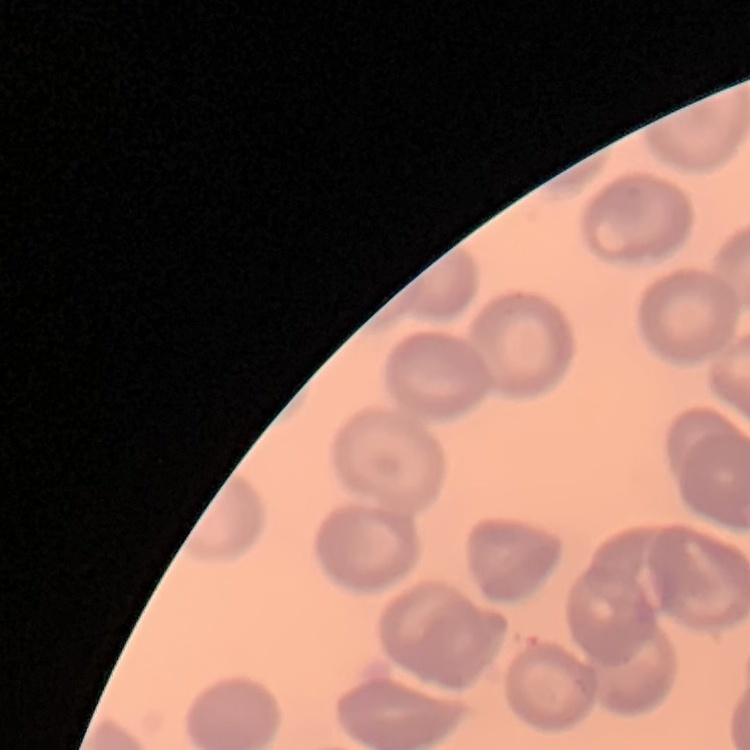

erythrocyte morphology = no rouleaux formation
image type = one tile cut from a larger photomicrograph
preparation = thin blood film
stain = Field's or Giemsa